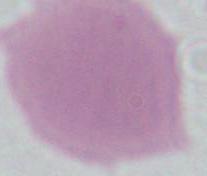

{
  "identification": "erythrocyte",
  "magnification": "1000x",
  "modality": "photomicrograph"
}